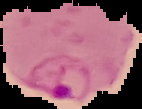
Cell region segmented out of the field of view; the surrounding area is masked to black. Result: Plasmodium parasites detected. Image is 142×109 pixels. From a thin blood film.